Identify the cell.
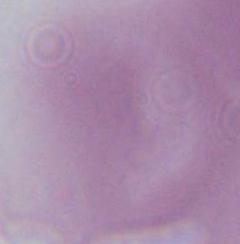
This is an erythrocyte.

1000x magnification. Photomicrograph.